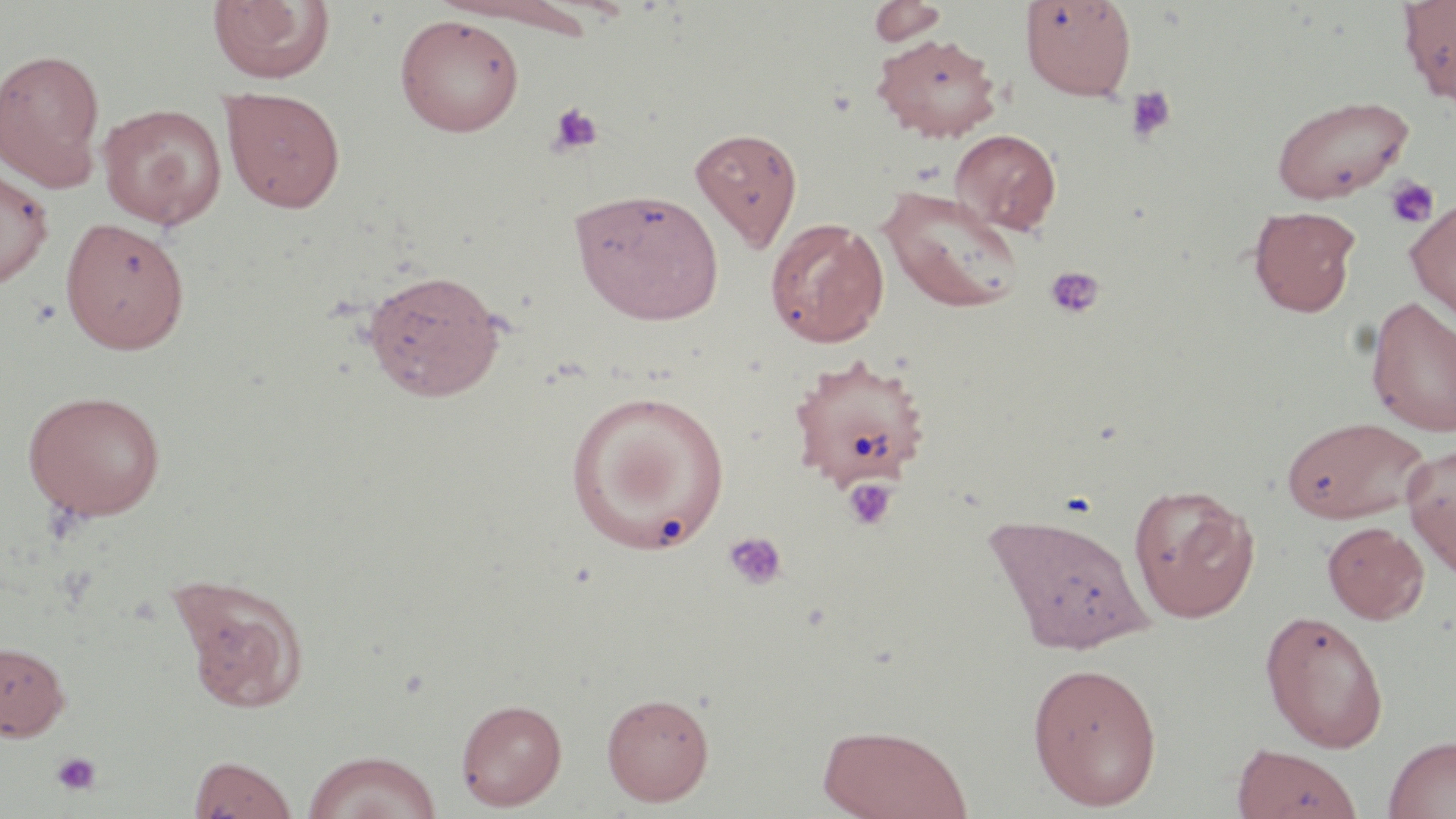

slide-level diagnosis = negative for blood parasites
image size = 1456×819 pixels
field of view = one of a larger specimen
platelet locations = approximate bounding boxes as [x1, y1, x2, y2] in pixels: [1126, 86, 1176, 144], [547, 102, 604, 156], [1384, 176, 1439, 229], [1045, 266, 1106, 320], [842, 478, 897, 532], [723, 531, 788, 592], [50, 750, 102, 797]
stain = May-Grünwald-Giemsa
modality = optical microscopy
preparation = thin blood smear
magnification = 1000x
uninfected red blood cell locations = approximate bounding boxes as [x1, y1, x2, y2] in pixels: [207, 0, 336, 86], [1397, 0, 1456, 104], [434, 1, 600, 36], [867, 1, 947, 47], [1020, 1, 1137, 100], [394, 13, 525, 137], [871, 32, 1003, 142], [0, 47, 106, 189], [220, 86, 346, 212], [1271, 94, 1414, 204], [98, 103, 227, 228], [690, 127, 803, 250], [950, 129, 1062, 236], [0, 167, 55, 288], [878, 184, 1025, 313], [570, 187, 725, 325], [1405, 195, 1456, 323], [1249, 206, 1361, 317], [60, 216, 190, 355], [764, 217, 890, 348], [360, 268, 507, 402], [1366, 297, 1456, 437], [788, 353, 933, 491], [22, 389, 168, 522], [566, 389, 731, 551], [1281, 415, 1430, 524], [1402, 444, 1456, 576], [1128, 483, 1259, 623], [982, 510, 1157, 656], [1322, 521, 1429, 624], [168, 571, 312, 713], [1259, 609, 1388, 752], [0, 642, 70, 741], [1026, 660, 1163, 809], [601, 692, 715, 806], [455, 698, 567, 811], [816, 722, 973, 818], [1383, 735, 1456, 819], [1232, 744, 1364, 818], [301, 750, 442, 819], [187, 755, 298, 818]